State the preparation type.
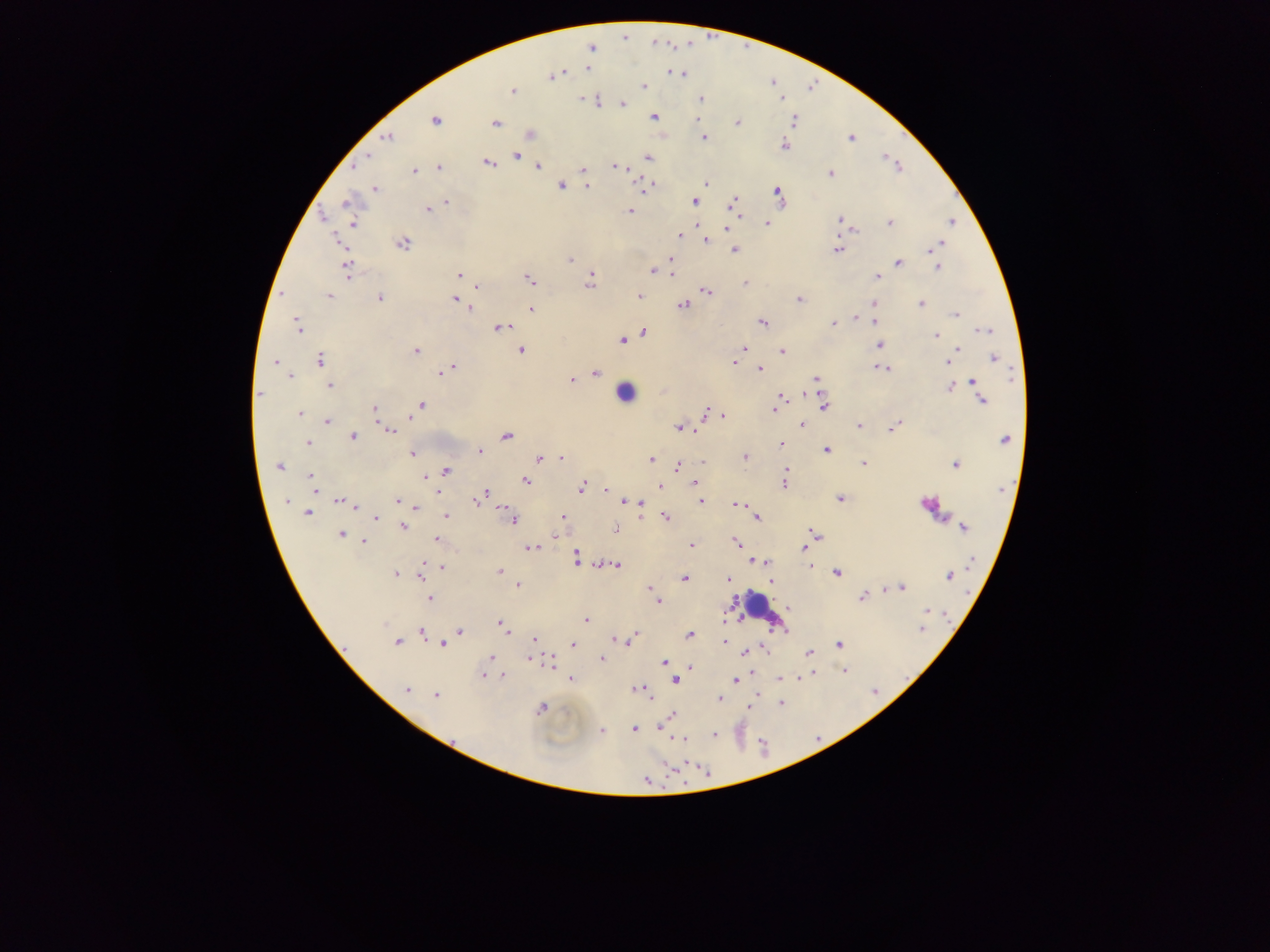
Thick blood film.

leukocyte_locations: 'approximate centers as x y in pixels: 625 392; 761 611'
plasmodium_parasite_locations: 'approximate centers as x y in pixels: 624 36; 591 48; 587 68; 672 73; 681 73; 551 75; 644 86; 510 90; 701 99; 781 99; 583 100; 597 100; 622 103; 654 117; 435 120; 737 122; 793 122; 495 123; 530 134; 386 136; 702 137; 851 137; 784 145; 516 155; 884 156; 647 157; 518 159; 487 162; 357 163; 615 166; 537 167; 898 167; 440 168; 414 170; 582 171; 830 173; 705 183; 560 185; 587 186; 649 186; 643 187; 374 189; 778 194; 693 201; 447 202; 733 203; 348 204; 427 209; 631 211; 740 216; 839 221; 950 222; 352 223; 889 223; 767 224; 725 228; 852 229; 678 235; 705 241; 402 243; 937 244; 733 249; 837 249; 671 256; 569 259; 898 263; 938 267; 347 269; 653 271; 671 272; 459 275; 877 276; 529 279; 590 281; 745 283; 476 286; 705 291; 282 294; 328 295; 638 295; 379 297; 455 298; 798 299; 874 303; 921 303; 683 304; 471 308; 531 309; 955 313; 855 318; 874 321; 762 322; 833 323; 297 325; 499 327; 984 330; 642 333; 936 335; 622 339; 879 345; 958 348; 742 349; 521 350; 415 351; 781 351; 993 358; 275 361; 320 361; 949 361; 733 362; 882 367; 451 369; 759 370; 444 371; 596 373; 288 376; 817 378; 571 379; 972 382; 329 385; 949 387; 802 392; 260 393; 783 395; 981 400; 823 405; 420 406; 374 409; 773 409; 705 412; 299 413; 721 415; 409 416; 327 422; 802 424; 860 425; 893 427; 679 428; 389 430; 695 430; 351 436; 506 436; 1004 440; 306 443; 781 443; 827 449; 479 451; 412 453; 744 457; 539 458; 561 458; 651 458; 702 462; 864 463; 955 464; 279 466; 676 466; 787 469; 444 471; 785 476; 312 477; 425 478; 526 481; 693 482; 784 484; 312 486; 659 486; 580 488; 605 489; 440 492; 482 495; 840 498; 288 501; 700 501; 342 502; 397 502; 623 502; 632 502; 737 503; 929 503; 638 504; 355 506; 416 507; 307 513; 446 515; 665 516; 375 517; 562 518; 639 518; 755 519; 512 520; 402 526; 963 527; 616 529; 816 533; 341 534; 554 535; 436 539; 363 541; 736 542; 691 545; 532 548; 804 548; 576 557; 972 559; 751 561; 757 561; 765 561; 441 565; 616 565; 811 567; 433 568; 499 571; 836 572; 396 574; 421 574; 948 576; 683 578; 727 581; 771 582; 518 585; 647 588; 901 588; 883 590; 652 593; 861 597; 430 598; 658 600; 789 607; 925 610; 725 618; 585 621; 500 624; 921 629; 421 631; 459 631; 636 633; 689 635; 632 637; 534 638; 614 639; 397 641; 725 641; 441 644; 573 644; 837 644; 764 648; 743 652; 808 652; 490 657; 530 660; 601 660; 663 662; 550 663; 690 667; 846 671; 814 672; 482 675; 504 676; 797 677; 571 678; 779 678; 734 680; 675 681; 635 688; 642 688; 406 689; 647 692; 758 694; 436 695; 719 699; 780 703; 541 708; 749 708; 672 715; 660 727; 634 728; 601 731; 714 734; 675 739; 684 739'
country: Ghana
capture: mobile-phone photograph through a microscope
image_size: 1270×952 pixels
field_of_view: single